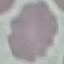 Malaria status: uninfected. Automatically extracted cell patch, resized to 64 × 64 pixels. Thin blood smear. Giemsa stain. Photographed with a smartphone camera at the microscope eyepiece.